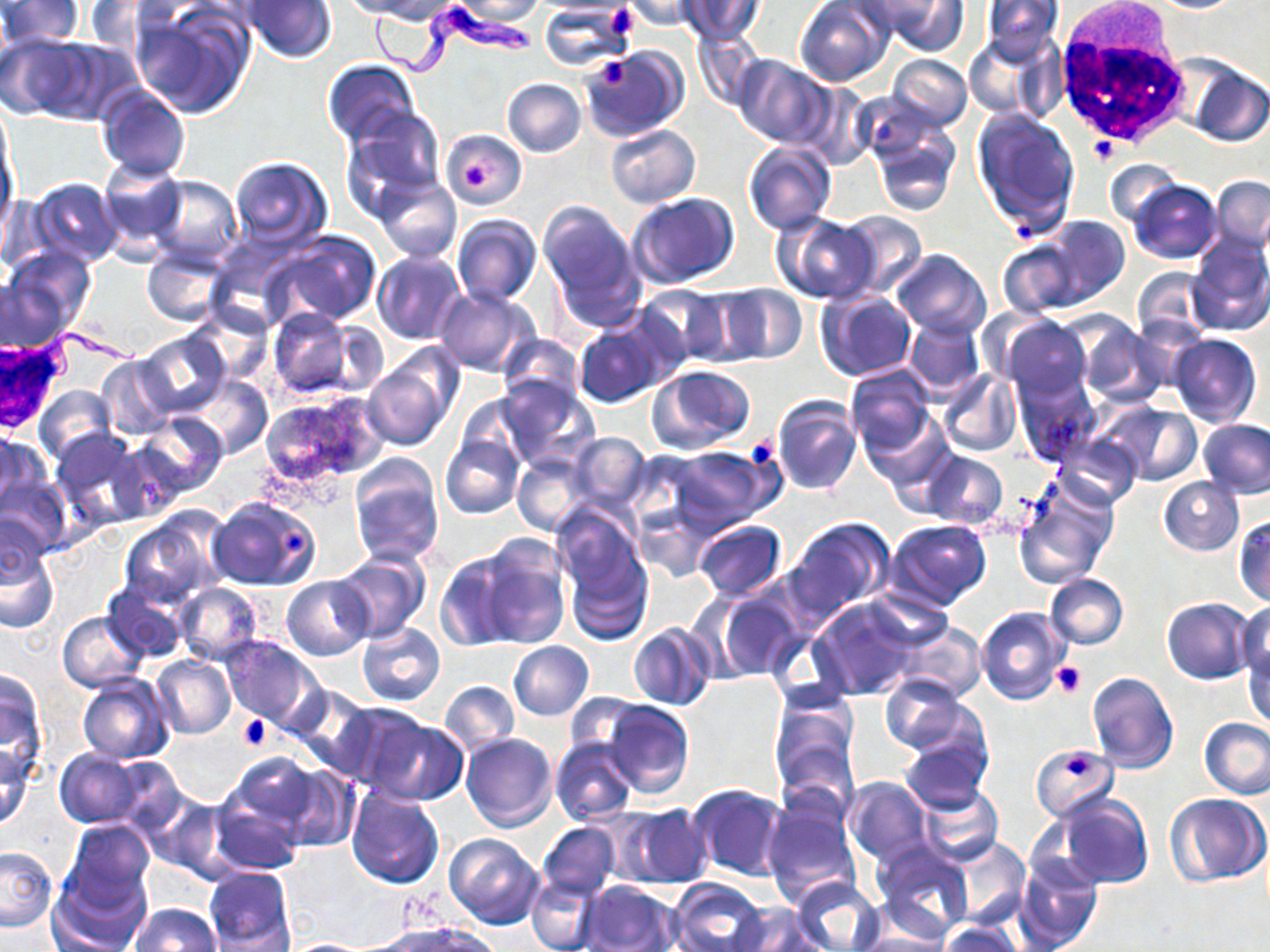

Summary:
  - Coordinate format: approximate bounding boxes as (x1, y1, x2, y2) in pixels
  - Trypanosoma brucei locations: (361, 6, 545, 91)
  - White blood cell locations: (1051, 10, 1194, 148)
  - Platelet locations: (605, 4, 640, 41), (593, 55, 631, 92), (1089, 137, 1117, 163), (463, 163, 494, 190), (743, 433, 782, 476), (280, 528, 308, 559), (1052, 661, 1084, 698), (238, 714, 273, 750), (1067, 753, 1091, 778)
  - Uninfected red blood cell locations: (2, 0, 83, 48), (343, 0, 438, 19), (454, 0, 545, 23), (622, 0, 703, 31), (676, 0, 763, 44), (796, 0, 893, 86), (857, 0, 965, 52), (979, 0, 1064, 67), (1150, 0, 1242, 13), (82, 1, 161, 51), (244, 1, 337, 63), (541, 2, 637, 71), (131, 3, 255, 119), (691, 30, 763, 110), (0, 33, 93, 121), (963, 35, 1052, 121), (582, 45, 688, 142), (887, 55, 972, 131), (734, 56, 830, 148), (323, 59, 420, 146), (1182, 61, 1269, 150), (503, 78, 586, 157), (95, 85, 190, 181), (972, 108, 1079, 235), (342, 110, 445, 213), (869, 124, 959, 218), (605, 125, 700, 207), (442, 129, 527, 208), (743, 141, 836, 236), (227, 155, 332, 248), (97, 159, 188, 258), (1105, 159, 1181, 227), (375, 175, 461, 263), (149, 176, 242, 268), (1210, 176, 1270, 254), (29, 178, 123, 266), (1129, 180, 1222, 263), (628, 193, 739, 291), (537, 200, 639, 321), (834, 210, 929, 298), (773, 213, 880, 304), (452, 214, 542, 307), (1037, 214, 1131, 308), (265, 230, 382, 327), (1187, 233, 1270, 335), (997, 241, 1083, 320), (5, 247, 94, 334), (890, 249, 990, 340), (143, 250, 228, 326), (372, 251, 464, 344), (1132, 266, 1212, 344), (0, 276, 71, 352), (715, 284, 808, 365), (639, 285, 733, 365), (434, 286, 537, 375), (676, 288, 763, 366), (817, 291, 916, 382), (268, 310, 367, 401), (1001, 316, 1091, 402), (1068, 316, 1165, 404), (574, 317, 667, 408), (902, 317, 986, 397), (134, 330, 230, 418), (497, 333, 584, 406), (1170, 334, 1261, 428), (95, 356, 178, 441), (363, 362, 452, 452), (844, 364, 936, 458), (648, 365, 756, 452), (938, 369, 1023, 457), (1012, 375, 1096, 463), (185, 376, 272, 460), (496, 376, 600, 473), (34, 386, 118, 465), (259, 394, 387, 489), (457, 394, 534, 473), (771, 395, 862, 497), (1106, 404, 1201, 485), (865, 411, 952, 497), (136, 412, 228, 496), (1200, 418, 1270, 496), (50, 428, 147, 526), (0, 431, 45, 518), (566, 433, 651, 512), (442, 434, 524, 519), (1055, 435, 1143, 509), (109, 441, 187, 523), (666, 445, 777, 534), (924, 451, 1008, 529), (513, 454, 593, 535), (350, 456, 444, 566), (1, 473, 70, 559), (1158, 477, 1244, 556), (1015, 482, 1116, 589), (207, 497, 321, 590), (553, 508, 653, 639), (1, 513, 49, 591), (119, 515, 221, 608), (1233, 515, 1270, 606), (785, 518, 893, 622), (886, 520, 993, 612), (692, 521, 786, 599), (475, 537, 571, 650), (0, 547, 59, 633), (331, 552, 429, 644), (434, 554, 515, 653), (1043, 573, 1128, 649), (282, 574, 373, 660), (173, 581, 263, 665), (101, 586, 186, 661), (708, 589, 807, 681), (812, 596, 920, 700), (1162, 597, 1255, 685), (1234, 601, 1270, 678), (976, 607, 1070, 704), (59, 612, 148, 692), (892, 620, 985, 704), (357, 621, 445, 706), (627, 623, 715, 711), (221, 636, 322, 729), (508, 641, 594, 720), (1244, 642, 1270, 730), (151, 655, 236, 739), (0, 667, 49, 781), (1085, 671, 1178, 774), (77, 673, 175, 762), (879, 675, 971, 756), (439, 680, 519, 756), (288, 686, 379, 779), (312, 698, 420, 789), (602, 700, 694, 799), (770, 700, 858, 797), (1200, 717, 1270, 798), (362, 718, 468, 805), (462, 733, 557, 831), (901, 734, 992, 816), (549, 736, 637, 825), (1031, 743, 1119, 822), (1, 744, 35, 830), (54, 749, 148, 828), (223, 752, 325, 842), (105, 757, 188, 833), (273, 766, 359, 853), (844, 777, 931, 865), (687, 783, 789, 883), (346, 787, 445, 889), (918, 787, 1003, 866), (208, 791, 306, 876), (143, 792, 235, 880), (1057, 793, 1154, 887), (1165, 794, 1268, 885), (762, 801, 861, 908), (617, 803, 713, 889), (65, 818, 154, 904), (538, 822, 620, 897), (444, 833, 545, 929), (950, 839, 1030, 929), (872, 841, 974, 938), (1, 845, 56, 932), (1015, 853, 1102, 951), (50, 863, 151, 952), (204, 866, 295, 950), (791, 875, 885, 952), (525, 876, 599, 951), (669, 879, 768, 952), (578, 880, 680, 952), (729, 902, 822, 952), (130, 903, 222, 952), (379, 921, 497, 951), (937, 922, 1022, 952), (854, 930, 953, 952), (277, 939, 378, 951)
  - Slide-level diagnosis: Trypanosoma brucei
  - Preparation: thin blood film
  - Magnification: 1000x
  - Field of view: one of a larger specimen
  - Modality: light microscopy
  - Stain: May-Grünwald-Giemsa
  - Image size: 1270×952 pixels